Identify the parasite.
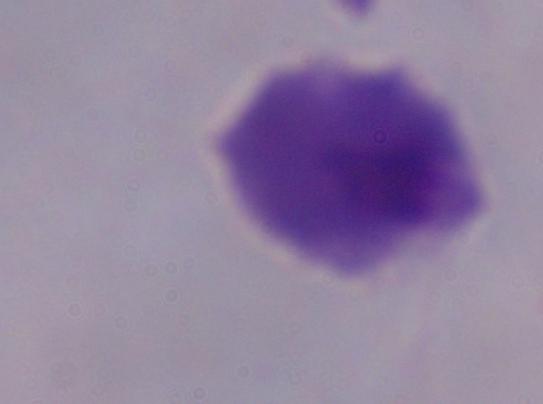

A trichomonad.

Micrograph. 1000x magnification.